Name the parasite shown.
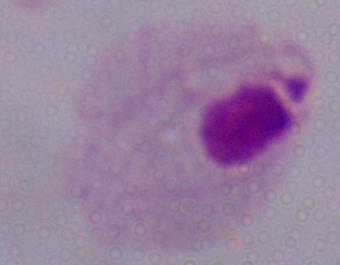
This is a trichomonad.

magnification = 1000x
modality = micrograph